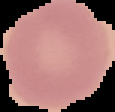

{
  "result": "no Plasmodium parasites seen",
  "image_type": "cell region segmented out of the field of view; surrounding area masked to black",
  "image_size": "115×112 pixels",
  "preparation": "thin blood smear"
}